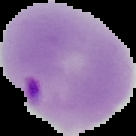

Image is 136×136 pixels. From a thin blood smear. The area outside the segmented cell region is set to black. Result: malaria parasites detected.